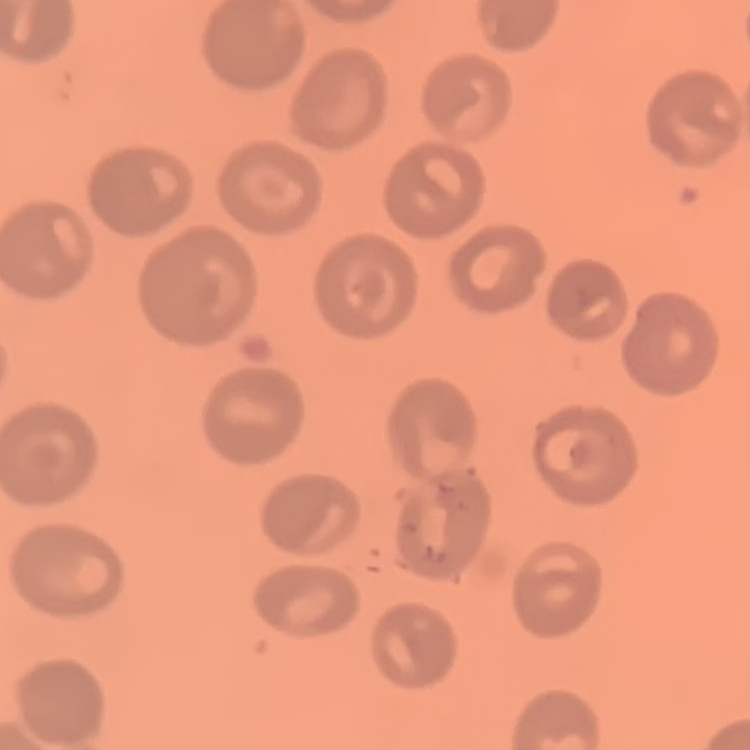
erythrocyte morphology = no rouleaux formation
stain = Field's or Giemsa
image type = one tile cut from a larger photomicrograph
preparation = thin blood smear